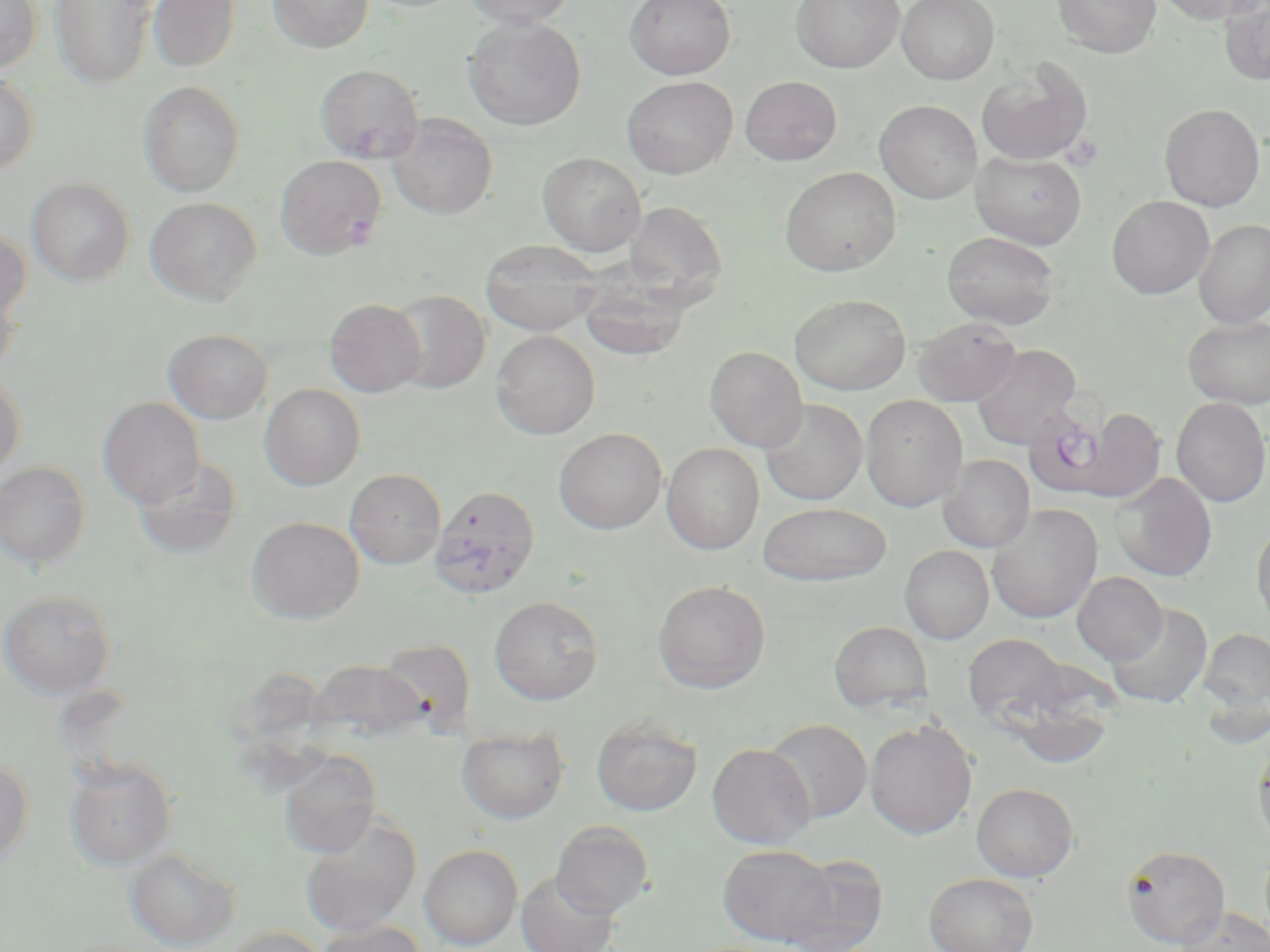
Approximate bounding boxes as [x1, y1, x2, y2] in pixels. Plasmodium falciparum-infected red blood cell locations: [1029, 390, 1126, 491], [429, 485, 540, 599]. Uninfected red blood cell locations: [0, 0, 41, 72], [50, 0, 157, 90], [147, 0, 240, 72], [268, 0, 373, 53], [461, 0, 576, 28], [624, 0, 736, 80], [790, 0, 904, 73], [897, 0, 999, 85], [1052, 0, 1161, 58], [1152, 0, 1268, 25], [1219, 1, 1270, 85], [464, 16, 586, 131], [977, 59, 1093, 165], [314, 64, 424, 163], [0, 75, 39, 174], [622, 75, 738, 178], [739, 76, 842, 166], [138, 81, 245, 197], [875, 99, 982, 204], [1159, 103, 1265, 211], [388, 114, 497, 219], [538, 151, 646, 255], [971, 151, 1087, 249], [276, 155, 385, 260], [780, 166, 901, 276], [26, 178, 134, 285], [1107, 195, 1214, 299], [145, 197, 262, 304], [623, 201, 727, 301], [1194, 219, 1270, 328], [0, 227, 31, 326], [941, 231, 1061, 330], [481, 239, 603, 337], [577, 270, 695, 362], [0, 278, 21, 373], [388, 289, 490, 393], [791, 293, 911, 395], [324, 298, 426, 397], [1183, 316, 1270, 409], [914, 317, 1021, 405], [164, 329, 272, 423], [491, 330, 600, 439], [972, 344, 1082, 449], [705, 346, 808, 452], [0, 372, 25, 477], [260, 384, 365, 490], [860, 395, 968, 511], [98, 397, 205, 508], [1170, 397, 1270, 508], [760, 399, 867, 505], [1069, 408, 1167, 504], [554, 428, 667, 534], [661, 443, 764, 554], [938, 454, 1034, 553], [133, 455, 243, 558], [0, 461, 91, 570], [344, 469, 446, 569], [1112, 473, 1217, 581], [757, 502, 893, 586], [987, 505, 1103, 624], [246, 516, 364, 623], [1251, 519, 1270, 632], [900, 545, 994, 644], [1072, 572, 1167, 665], [652, 580, 771, 693], [0, 589, 116, 699], [489, 596, 603, 705], [1106, 603, 1212, 708], [829, 620, 933, 714], [1199, 628, 1270, 715], [962, 633, 1070, 726], [377, 638, 477, 734], [308, 659, 426, 746], [1003, 693, 1117, 769], [591, 714, 703, 816], [765, 718, 872, 824], [864, 719, 977, 840], [456, 726, 569, 825], [1252, 740, 1270, 852], [706, 743, 816, 848], [278, 751, 380, 858], [0, 756, 34, 868], [64, 757, 177, 870], [972, 782, 1079, 881], [298, 813, 421, 937], [551, 820, 654, 917], [419, 844, 522, 950], [718, 844, 836, 946], [1121, 844, 1230, 948], [124, 847, 241, 950], [781, 853, 887, 952], [516, 871, 619, 952], [924, 872, 1039, 952], [1174, 906, 1270, 952], [315, 921, 427, 952], [221, 926, 333, 952]. Slide-level diagnosis: Plasmodium falciparum. Single field of view. Thin blood smear. Light microscopy. Image is 1270×952 pixels. Captured at 1000x magnification. May-Grünwald-Giemsa stain.